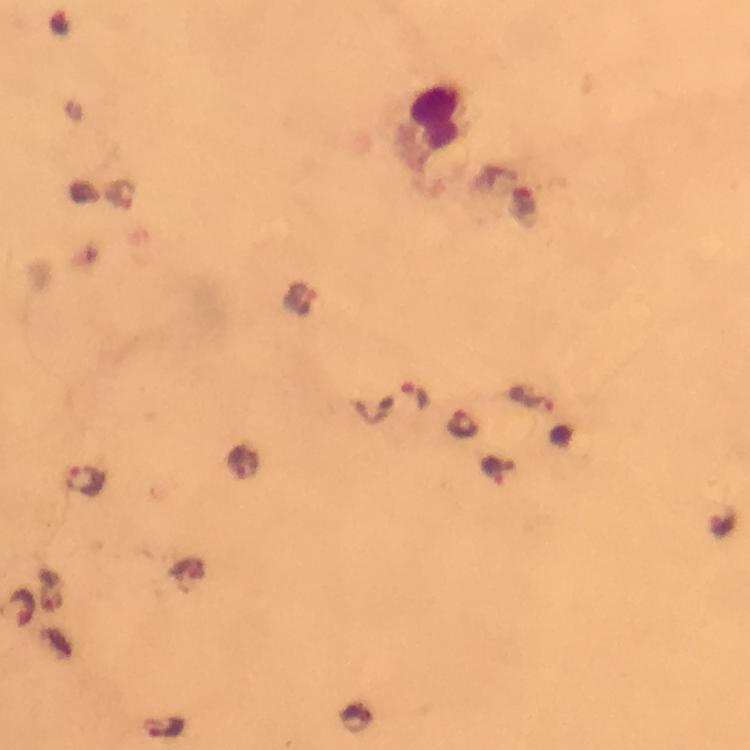

Approximate object centers, in pixels from the top-left corner. Malaria parasite locations: (x=119, y=193), (x=301, y=300), (x=416, y=396), (x=527, y=399), (x=463, y=423), (x=243, y=462), (x=492, y=470), (x=87, y=480), (x=723, y=522), (x=166, y=728). Leukocyte locations: (x=438, y=114). Image is 750×750 pixels. Thick blood film. Giemsa stain. Smartphone photograph taken through a microscope. Immersion oil was used. 100x magnification. From a malaria diagnostic workup. Cropped region of a single field of view.